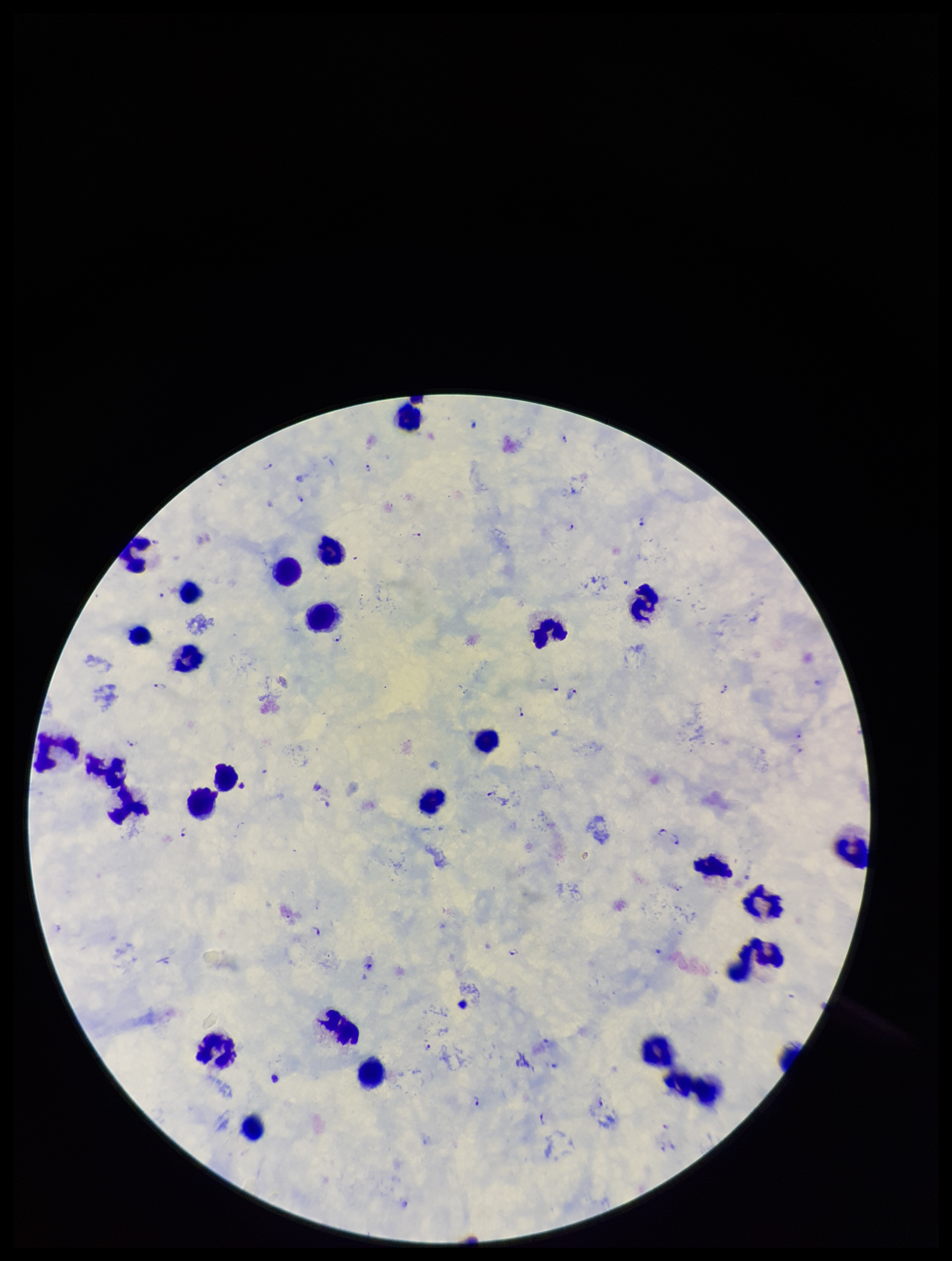
Summary:
  - Species reported for this patient: Plasmodium falciparum
  - Capture: smartphone photograph through the microscope eyepiece
  - Image size: 952×1261 pixels
  - Stain: Giemsa
  - Preparation: thick
  - Patient malaria status: infected
  - Leukocyte count: 26
  - Plasmodium parasites: detected
  - Field of view: single
  - Parasite count: 30